Describe the morphology of the erythrocytes.
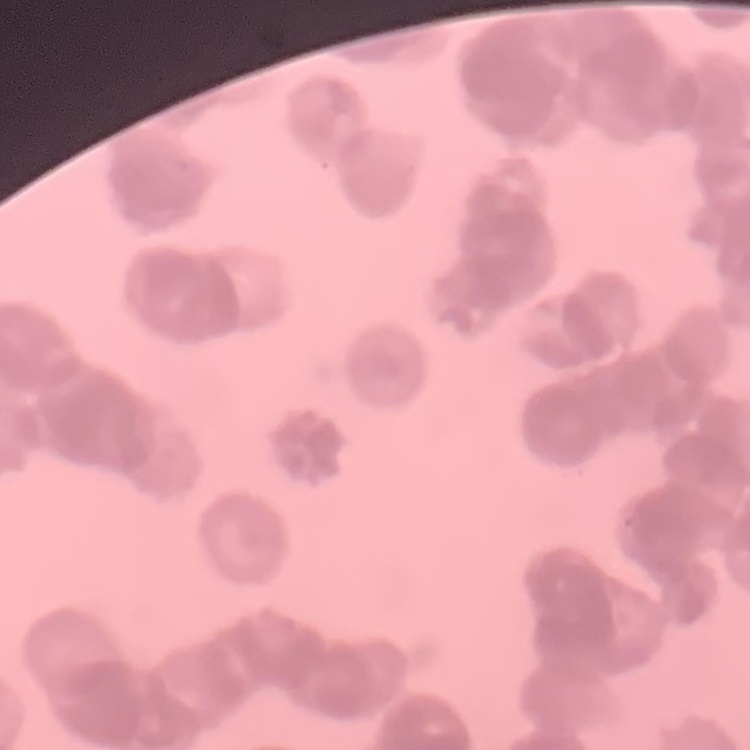

Rouleaux formation.

Field's or Giemsa stain. Thin blood smear. One tile cut from a larger photomicrograph.